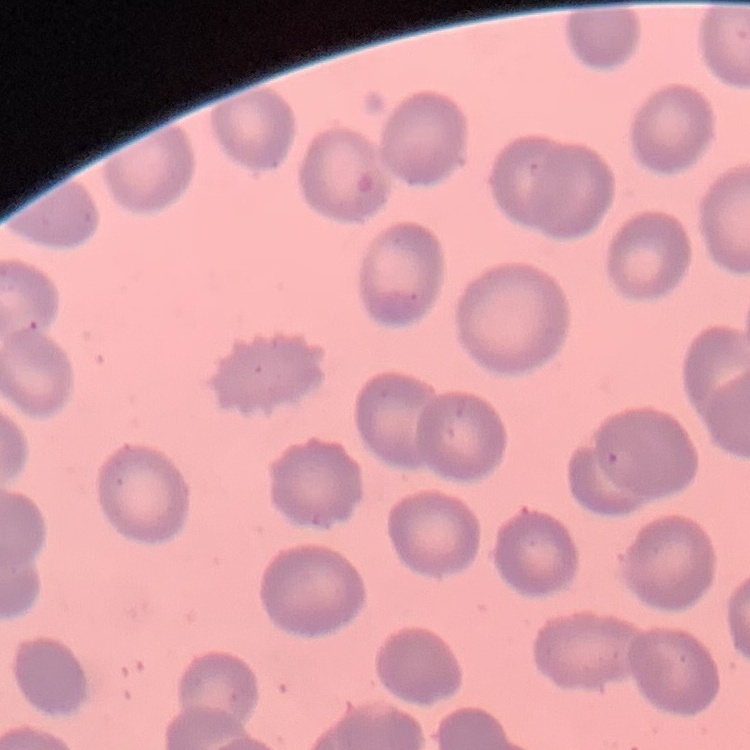

Summary:
  - Erythrocyte morphology: no rouleaux formation
  - Image type: one tile cut from a larger photomicrograph
  - Preparation: thin blood film
  - Stain: Field's or Giemsa